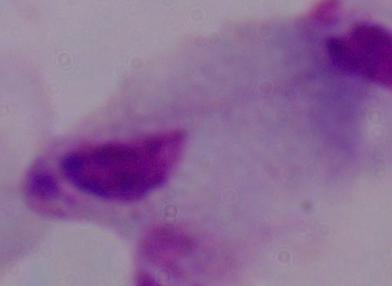

modality: photomicrograph
identification: trichomonad
magnification: 1000x